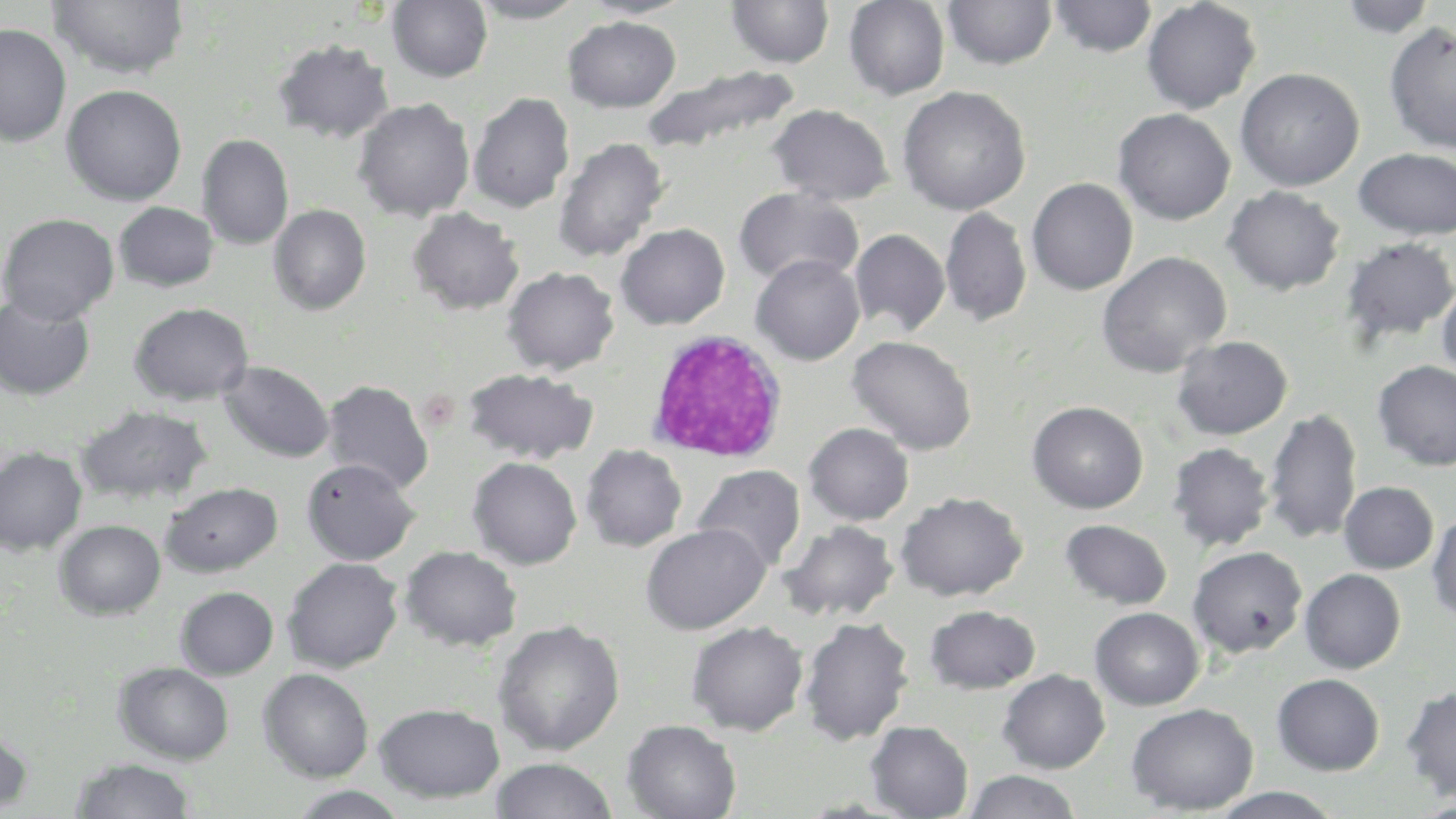

Summary:
  - Coordinate format: approximate bounding boxes as (x1, y1, x2, y2) in pixels
  - White blood cell locations: (646, 330, 789, 465)
  - Uninfected red blood cell locations: (49, 0, 189, 80), (468, 0, 588, 23), (578, 0, 692, 19), (726, 0, 835, 68), (843, 0, 950, 100), (1049, 0, 1157, 58), (1141, 0, 1261, 114), (387, 1, 493, 83), (942, 1, 1057, 70), (1337, 1, 1439, 38), (562, 16, 681, 113), (1383, 21, 1456, 154), (0, 22, 72, 146), (272, 38, 395, 144), (639, 63, 801, 156), (1235, 67, 1364, 191), (61, 84, 187, 206), (897, 86, 1031, 216), (468, 91, 575, 213), (353, 97, 475, 222), (768, 103, 894, 206), (1113, 108, 1236, 225), (197, 134, 294, 250), (552, 137, 669, 264), (1353, 148, 1455, 239), (1026, 177, 1138, 295), (1222, 185, 1346, 295), (733, 187, 864, 288), (113, 201, 219, 293), (268, 204, 371, 315), (407, 207, 524, 315), (940, 207, 1031, 326), (0, 213, 119, 325), (615, 223, 730, 330), (849, 229, 951, 337), (1340, 236, 1456, 345), (1096, 251, 1232, 378), (751, 254, 865, 365), (502, 266, 620, 376), (1437, 278, 1456, 384), (0, 295, 96, 400), (129, 302, 253, 405), (846, 335, 977, 455), (1171, 335, 1292, 440), (1372, 360, 1456, 471), (219, 361, 334, 464), (462, 367, 598, 465), (321, 379, 434, 494), (1027, 401, 1148, 514), (75, 404, 213, 505), (1263, 409, 1362, 544), (803, 422, 914, 526), (1166, 442, 1275, 551), (580, 444, 688, 551), (0, 446, 87, 555), (467, 457, 582, 570), (301, 458, 420, 566), (693, 464, 805, 573), (161, 481, 283, 577), (1340, 482, 1439, 574), (895, 491, 1028, 602), (1426, 511, 1456, 627), (54, 519, 166, 620), (1060, 519, 1172, 610), (780, 520, 900, 622), (641, 523, 770, 635), (400, 546, 523, 651), (1187, 546, 1308, 658), (282, 556, 404, 673), (1300, 568, 1406, 673), (175, 586, 279, 680), (924, 605, 1041, 694), (1089, 607, 1204, 710), (798, 615, 915, 746), (492, 620, 626, 756), (686, 620, 808, 736), (114, 662, 235, 764), (258, 668, 374, 782), (997, 669, 1110, 773), (1271, 673, 1384, 775), (1401, 685, 1456, 803), (373, 702, 505, 803), (1126, 702, 1258, 815), (622, 719, 742, 819), (866, 720, 974, 818), (0, 723, 33, 816), (490, 757, 618, 818), (70, 758, 196, 818), (963, 770, 1082, 819), (287, 786, 411, 819), (1207, 788, 1345, 819)
  - Slide-level diagnosis: negative for blood parasites
  - Image size: 1456×819 pixels
  - Modality: light microscopy
  - Stain: May-Grünwald-Giemsa
  - Magnification: 1000x
  - Preparation: thin blood smear
  - Field of view: single